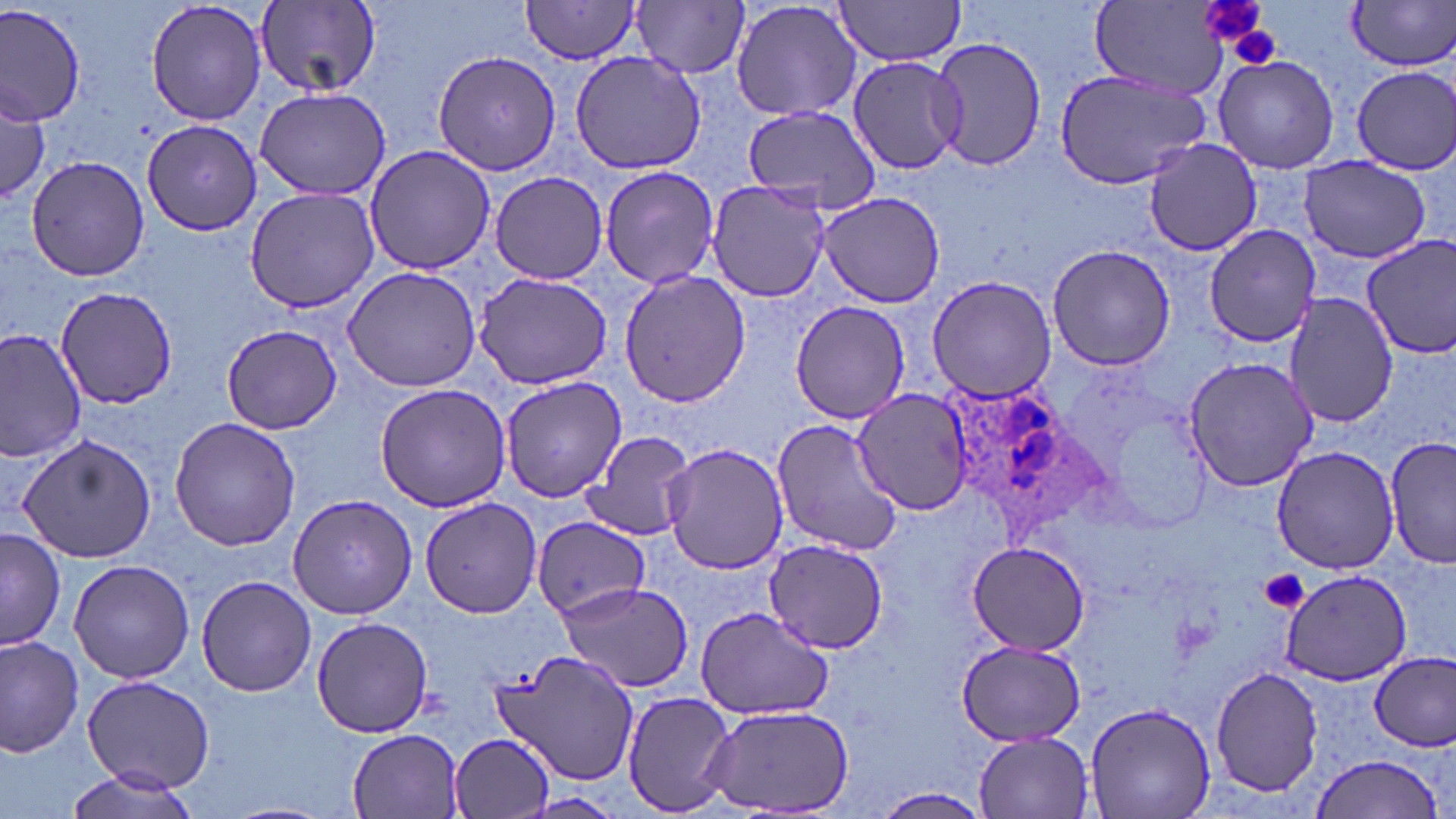

slide-level diagnosis = Plasmodium ovale
image size = 1456×819 pixels
preparation = thin blood film
uninfected red blood cell locations = approximate bounding boxes as named x1/y1/x2/y2 corners in pixels: (x1=731, y1=0, x2=863, y2=123), (x1=833, y1=0, x2=967, y2=66), (x1=1089, y1=0, x2=1236, y2=101), (x1=145, y1=1, x2=267, y2=127), (x1=254, y1=1, x2=383, y2=96), (x1=631, y1=1, x2=751, y2=79), (x1=1345, y1=1, x2=1456, y2=72), (x1=0, y1=2, x2=86, y2=125), (x1=518, y1=2, x2=644, y2=63), (x1=930, y1=37, x2=1050, y2=174), (x1=569, y1=49, x2=709, y2=175), (x1=431, y1=50, x2=563, y2=176), (x1=1213, y1=55, x2=1339, y2=172), (x1=845, y1=56, x2=966, y2=174), (x1=1351, y1=64, x2=1455, y2=172), (x1=1052, y1=67, x2=1211, y2=190), (x1=0, y1=86, x2=50, y2=199), (x1=254, y1=86, x2=391, y2=202), (x1=738, y1=105, x2=884, y2=217), (x1=142, y1=120, x2=263, y2=238), (x1=1141, y1=139, x2=1265, y2=256), (x1=362, y1=144, x2=494, y2=276), (x1=24, y1=155, x2=149, y2=282), (x1=1301, y1=157, x2=1431, y2=263), (x1=599, y1=164, x2=720, y2=289), (x1=488, y1=172, x2=611, y2=282), (x1=705, y1=180, x2=833, y2=303), (x1=244, y1=187, x2=379, y2=316), (x1=817, y1=192, x2=948, y2=309), (x1=1202, y1=225, x2=1323, y2=348), (x1=1360, y1=237, x2=1456, y2=358), (x1=1046, y1=244, x2=1176, y2=371), (x1=341, y1=264, x2=482, y2=393), (x1=618, y1=268, x2=749, y2=410), (x1=472, y1=270, x2=615, y2=390), (x1=925, y1=276, x2=1058, y2=403), (x1=57, y1=284, x2=179, y2=408), (x1=1283, y1=291, x2=1397, y2=429), (x1=788, y1=299, x2=911, y2=425), (x1=222, y1=324, x2=342, y2=435), (x1=0, y1=328, x2=87, y2=461), (x1=1183, y1=355, x2=1319, y2=492), (x1=500, y1=375, x2=627, y2=503), (x1=376, y1=382, x2=512, y2=512), (x1=850, y1=389, x2=976, y2=514), (x1=169, y1=416, x2=300, y2=551), (x1=771, y1=419, x2=904, y2=558), (x1=579, y1=431, x2=697, y2=540), (x1=13, y1=432, x2=158, y2=562), (x1=1385, y1=439, x2=1455, y2=570), (x1=662, y1=441, x2=789, y2=575), (x1=1271, y1=444, x2=1399, y2=574), (x1=287, y1=494, x2=417, y2=619), (x1=420, y1=498, x2=543, y2=618), (x1=531, y1=517, x2=651, y2=619), (x1=1, y1=527, x2=65, y2=653), (x1=764, y1=539, x2=888, y2=654), (x1=965, y1=542, x2=1092, y2=656), (x1=67, y1=559, x2=197, y2=684), (x1=1276, y1=570, x2=1414, y2=685), (x1=196, y1=575, x2=318, y2=697), (x1=556, y1=581, x2=696, y2=690), (x1=695, y1=607, x2=834, y2=719), (x1=312, y1=616, x2=433, y2=738), (x1=0, y1=633, x2=84, y2=756), (x1=955, y1=641, x2=1089, y2=746), (x1=493, y1=649, x2=643, y2=786), (x1=1370, y1=651, x2=1455, y2=752), (x1=1210, y1=667, x2=1322, y2=795), (x1=81, y1=676, x2=214, y2=791), (x1=622, y1=689, x2=736, y2=816), (x1=1085, y1=700, x2=1215, y2=819), (x1=700, y1=703, x2=858, y2=816), (x1=346, y1=728, x2=468, y2=819), (x1=973, y1=731, x2=1096, y2=817), (x1=450, y1=734, x2=557, y2=819), (x1=1309, y1=752, x2=1444, y2=819), (x1=60, y1=767, x2=207, y2=819), (x1=868, y1=788, x2=994, y2=819), (x1=222, y1=802, x2=338, y2=819)
Plasmodium ovale-infected red blood cell locations = approximate bounding boxes as named x1/y1/x2/y2 corners in pixels: (x1=939, y1=378, x2=1106, y2=536)
stain = May-Grünwald-Giemsa
field of view = one of a larger specimen
modality = light microscopy
magnification = 1000x
platelet locations = approximate bounding boxes as named x1/y1/x2/y2 corners in pixels: (x1=1199, y1=0, x2=1271, y2=54), (x1=1225, y1=21, x2=1285, y2=69), (x1=1261, y1=570, x2=1309, y2=614)